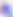

Photomicrograph. 400x magnification. Toxoplasma gondii is shown.